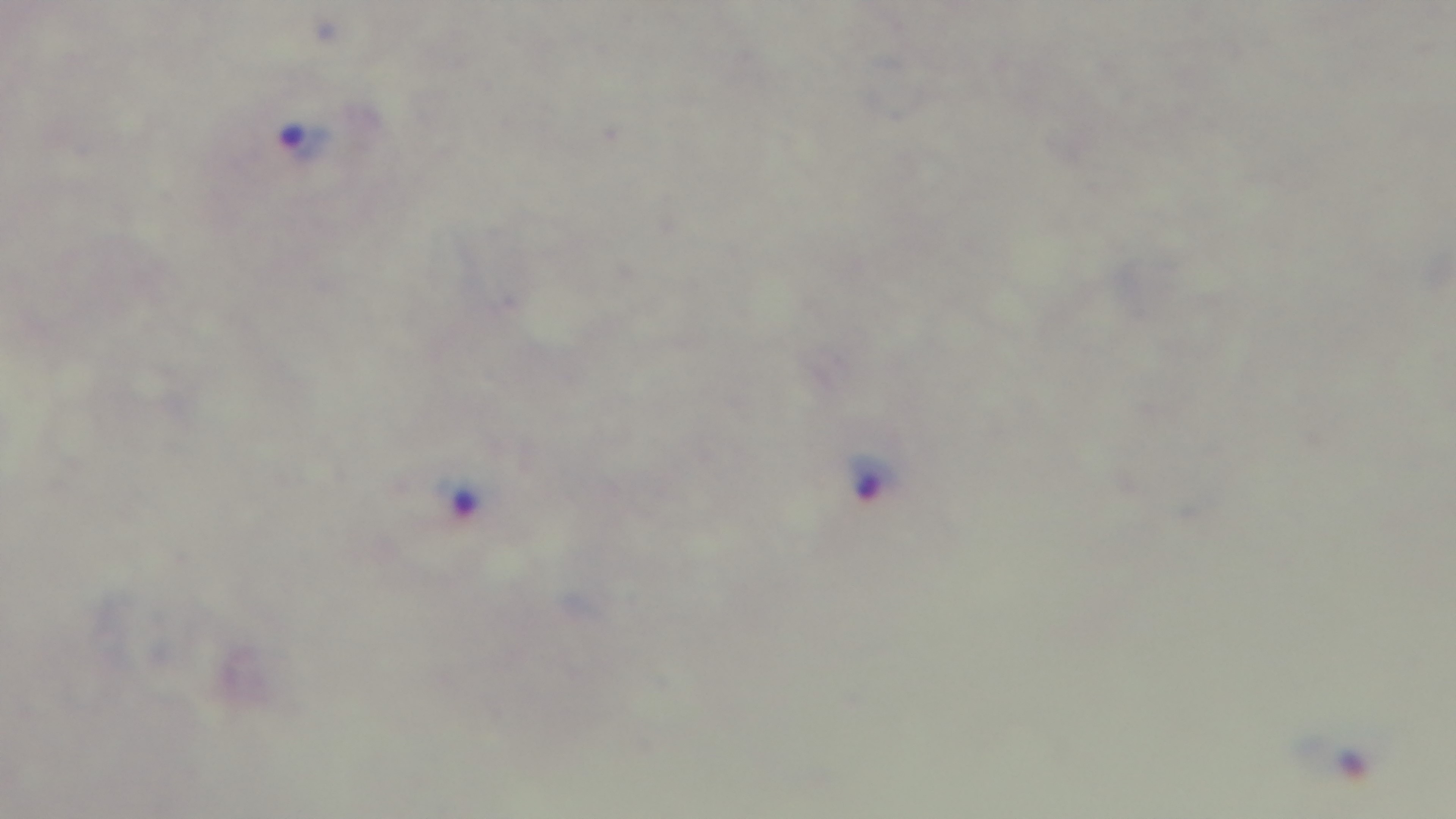

Giemsa stain. 100x oil-immersion objective. Malaria status: positive. Captured with a mounted 4K digital camera. Preparation: thick. Photomicrograph. One field from the slide.